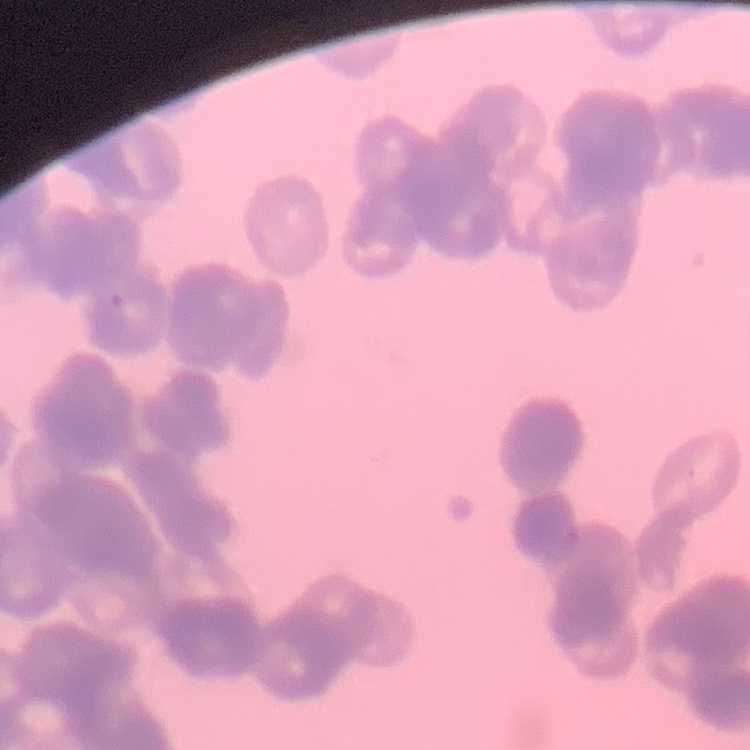
erythrocyte_morphology: rouleaux formation
stain: Field's or Giemsa
image_type: square crop of a larger photomicrograph
preparation: thin blood smear